Identify the blood parasite species.
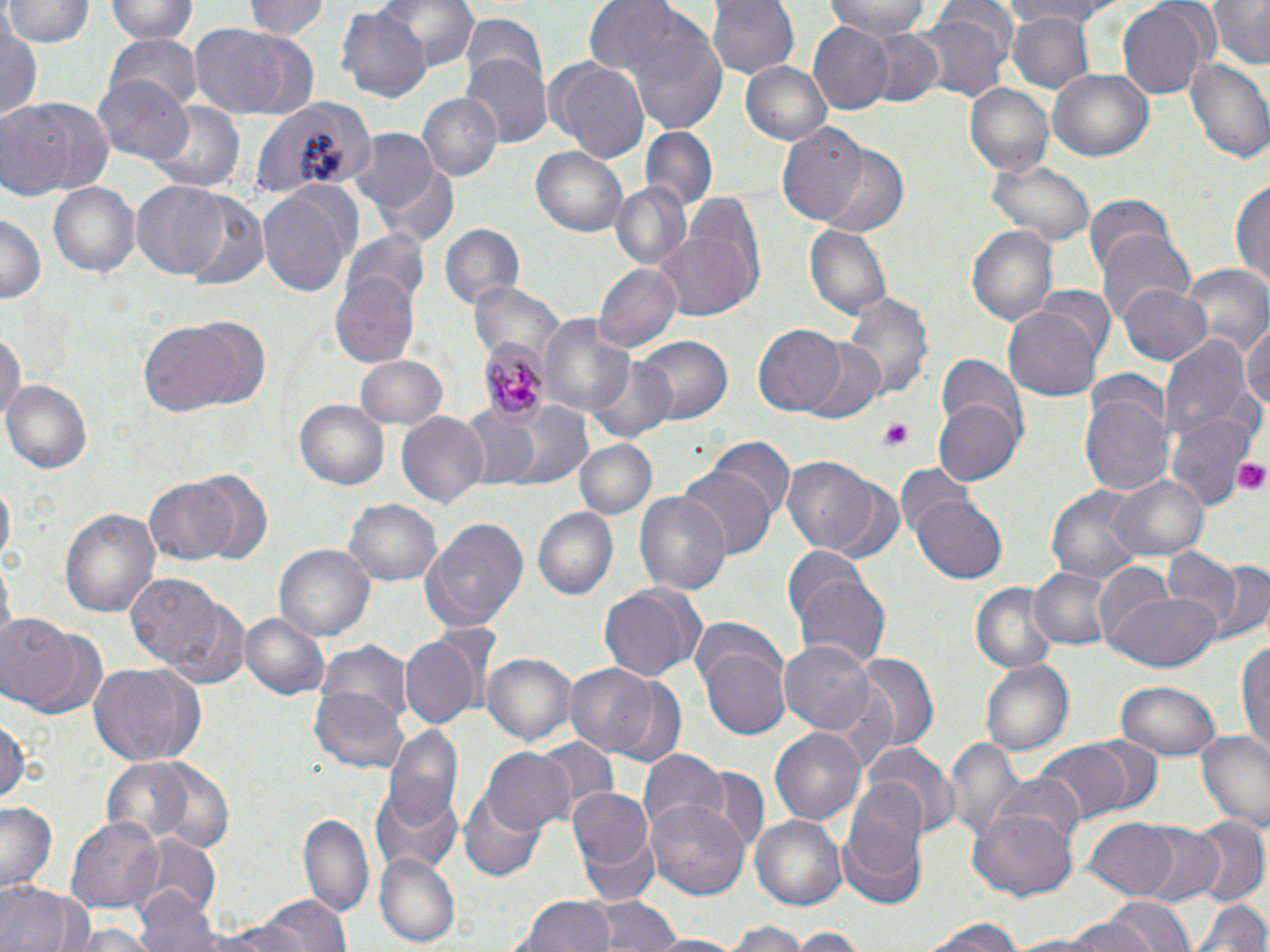
Plasmodium malariae.

Summary:
  - Coordinate format: approximate bounding boxes as named x1/y1/x2/y2 corners in pixels
  - Plasmodium malariae-infected red blood cell locations: (x1=479, y1=339, x2=549, y2=415)
  - Uninfected red blood cell locations: (x1=6, y1=0, x2=93, y2=50), (x1=105, y1=0, x2=201, y2=44), (x1=241, y1=0, x2=329, y2=41), (x1=380, y1=0, x2=479, y2=69), (x1=708, y1=0, x2=800, y2=79), (x1=823, y1=0, x2=935, y2=39), (x1=995, y1=0, x2=1121, y2=27), (x1=1206, y1=0, x2=1270, y2=66), (x1=1115, y1=1, x2=1211, y2=99), (x1=596, y1=5, x2=730, y2=132), (x1=334, y1=6, x2=430, y2=105), (x1=1007, y1=10, x2=1096, y2=94), (x1=913, y1=11, x2=1012, y2=103), (x1=1, y1=16, x2=42, y2=125), (x1=458, y1=17, x2=547, y2=97), (x1=187, y1=22, x2=320, y2=121), (x1=807, y1=23, x2=894, y2=113), (x1=859, y1=29, x2=943, y2=107), (x1=104, y1=34, x2=203, y2=114), (x1=463, y1=55, x2=552, y2=148), (x1=544, y1=58, x2=650, y2=162), (x1=1186, y1=58, x2=1270, y2=164), (x1=742, y1=61, x2=830, y2=144), (x1=1049, y1=69, x2=1155, y2=161), (x1=97, y1=76, x2=194, y2=167), (x1=963, y1=83, x2=1053, y2=179), (x1=419, y1=93, x2=502, y2=183), (x1=249, y1=95, x2=378, y2=203), (x1=0, y1=96, x2=114, y2=198), (x1=150, y1=104, x2=243, y2=192), (x1=776, y1=122, x2=867, y2=226), (x1=640, y1=128, x2=717, y2=214), (x1=349, y1=131, x2=440, y2=218), (x1=531, y1=147, x2=628, y2=238), (x1=817, y1=148, x2=908, y2=238), (x1=987, y1=161, x2=1096, y2=248), (x1=1231, y1=176, x2=1270, y2=292), (x1=131, y1=181, x2=232, y2=281), (x1=50, y1=182, x2=140, y2=279), (x1=615, y1=183, x2=690, y2=268), (x1=259, y1=186, x2=353, y2=300), (x1=1083, y1=194, x2=1177, y2=277), (x1=183, y1=197, x2=269, y2=292), (x1=654, y1=199, x2=766, y2=322), (x1=0, y1=212, x2=47, y2=307), (x1=438, y1=222, x2=526, y2=314), (x1=966, y1=224, x2=1058, y2=328), (x1=804, y1=225, x2=891, y2=323), (x1=1097, y1=231, x2=1197, y2=327), (x1=342, y1=232, x2=427, y2=314), (x1=594, y1=262, x2=681, y2=352), (x1=1182, y1=264, x2=1267, y2=356), (x1=330, y1=276, x2=419, y2=368), (x1=471, y1=280, x2=563, y2=361), (x1=1118, y1=283, x2=1214, y2=367), (x1=1033, y1=286, x2=1116, y2=366), (x1=841, y1=289, x2=936, y2=399), (x1=1003, y1=305, x2=1102, y2=403), (x1=540, y1=315, x2=635, y2=416), (x1=1243, y1=320, x2=1269, y2=417), (x1=138, y1=323, x2=243, y2=415), (x1=753, y1=324, x2=846, y2=418), (x1=0, y1=326, x2=25, y2=432), (x1=1160, y1=332, x2=1260, y2=449), (x1=635, y1=334, x2=734, y2=425), (x1=800, y1=341, x2=887, y2=425), (x1=355, y1=353, x2=449, y2=430), (x1=934, y1=354, x2=1027, y2=448), (x1=588, y1=357, x2=677, y2=442), (x1=3, y1=381, x2=92, y2=475), (x1=1080, y1=394, x2=1174, y2=496), (x1=294, y1=397, x2=390, y2=490), (x1=456, y1=399, x2=588, y2=491), (x1=933, y1=399, x2=1022, y2=485), (x1=1167, y1=413, x2=1253, y2=506), (x1=396, y1=414, x2=488, y2=507), (x1=575, y1=438, x2=656, y2=519), (x1=708, y1=438, x2=794, y2=521), (x1=783, y1=457, x2=881, y2=555), (x1=896, y1=464, x2=979, y2=542), (x1=676, y1=465, x2=776, y2=561), (x1=1108, y1=472, x2=1210, y2=562), (x1=190, y1=474, x2=275, y2=560), (x1=145, y1=478, x2=237, y2=564), (x1=1, y1=479, x2=16, y2=561), (x1=1047, y1=483, x2=1148, y2=583), (x1=635, y1=491, x2=730, y2=597), (x1=343, y1=496, x2=444, y2=588), (x1=912, y1=496, x2=1007, y2=584), (x1=60, y1=506, x2=161, y2=619), (x1=531, y1=506, x2=620, y2=600), (x1=421, y1=519, x2=530, y2=632), (x1=1160, y1=545, x2=1245, y2=635), (x1=275, y1=546, x2=373, y2=641), (x1=1187, y1=558, x2=1267, y2=647), (x1=784, y1=562, x2=892, y2=668), (x1=1092, y1=562, x2=1180, y2=655), (x1=1029, y1=566, x2=1116, y2=652), (x1=126, y1=574, x2=225, y2=668), (x1=972, y1=581, x2=1061, y2=673), (x1=599, y1=583, x2=704, y2=682), (x1=1108, y1=590, x2=1222, y2=673), (x1=168, y1=598, x2=252, y2=689), (x1=240, y1=612, x2=330, y2=699), (x1=0, y1=617, x2=79, y2=709), (x1=686, y1=620, x2=850, y2=733), (x1=399, y1=634, x2=480, y2=730), (x1=1236, y1=635, x2=1270, y2=759), (x1=780, y1=639, x2=879, y2=734), (x1=699, y1=641, x2=792, y2=742), (x1=316, y1=642, x2=414, y2=728), (x1=483, y1=651, x2=577, y2=746), (x1=855, y1=653, x2=939, y2=748), (x1=979, y1=659, x2=1073, y2=758), (x1=88, y1=663, x2=205, y2=764), (x1=564, y1=663, x2=661, y2=757), (x1=598, y1=675, x2=688, y2=769), (x1=1115, y1=679, x2=1221, y2=760), (x1=310, y1=689, x2=409, y2=773), (x1=0, y1=712, x2=28, y2=807), (x1=769, y1=724, x2=864, y2=823), (x1=383, y1=726, x2=464, y2=824), (x1=1195, y1=730, x2=1270, y2=832), (x1=532, y1=735, x2=617, y2=817), (x1=942, y1=735, x2=1023, y2=844), (x1=1035, y1=738, x2=1139, y2=826), (x1=865, y1=743, x2=959, y2=836), (x1=481, y1=748, x2=575, y2=836), (x1=640, y1=749, x2=726, y2=838), (x1=101, y1=760, x2=201, y2=845), (x1=674, y1=766, x2=765, y2=854), (x1=991, y1=772, x2=1085, y2=854), (x1=371, y1=784, x2=463, y2=873), (x1=570, y1=786, x2=658, y2=896), (x1=457, y1=787, x2=547, y2=881), (x1=841, y1=787, x2=928, y2=905), (x1=646, y1=797, x2=751, y2=898), (x1=0, y1=802, x2=59, y2=891), (x1=968, y1=807, x2=1079, y2=901), (x1=299, y1=811, x2=374, y2=921), (x1=751, y1=816, x2=848, y2=912), (x1=66, y1=818, x2=162, y2=908), (x1=1189, y1=818, x2=1269, y2=909), (x1=1086, y1=820, x2=1181, y2=899), (x1=1136, y1=823, x2=1227, y2=907), (x1=136, y1=838, x2=220, y2=921), (x1=376, y1=854, x2=459, y2=947), (x1=0, y1=881, x2=81, y2=952), (x1=137, y1=887, x2=224, y2=952), (x1=258, y1=895, x2=349, y2=952), (x1=518, y1=895, x2=614, y2=952), (x1=591, y1=895, x2=675, y2=952), (x1=1192, y1=895, x2=1268, y2=952), (x1=1104, y1=896, x2=1194, y2=952), (x1=1057, y1=912, x2=1149, y2=952), (x1=922, y1=916, x2=1032, y2=952), (x1=727, y1=922, x2=811, y2=952), (x1=790, y1=928, x2=864, y2=952), (x1=646, y1=934, x2=745, y2=952)
  - Platelet locations: (x1=878, y1=417, x2=916, y2=453), (x1=1232, y1=457, x2=1270, y2=496)
  - Field of view: one of a larger specimen
  - Stain: May-Grünwald-Giemsa
  - Magnification: 1000x
  - Image size: 1270×952 pixels
  - Preparation: thin blood smear
  - Modality: optical microscopy